Identify the parasite.
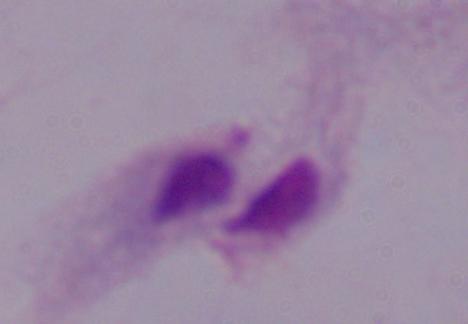

A trichomonad.

Captured at 1000x magnification. Photomicrograph.